State which cell type is depicted.
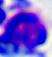
This is a leukocyte.

Captured at 400x magnification. Micrograph.